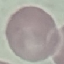
Summary:
  - Result: no malaria parasites detected
  - Preparation: thin blood film
  - Capture: smartphone through the microscope eyepiece
  - Image type: cell patch, automatically extracted from a larger field of view and resized to 64 × 64 pixels
  - Stain: Giemsa